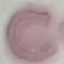

Summary:
  - Malaria status: uninfected
  - Stain: Giemsa
  - Capture: smartphone through the microscope eyepiece
  - Preparation: thin blood smear
  - Image type: automatically extracted cell patch, resized to 64 × 64 pixels